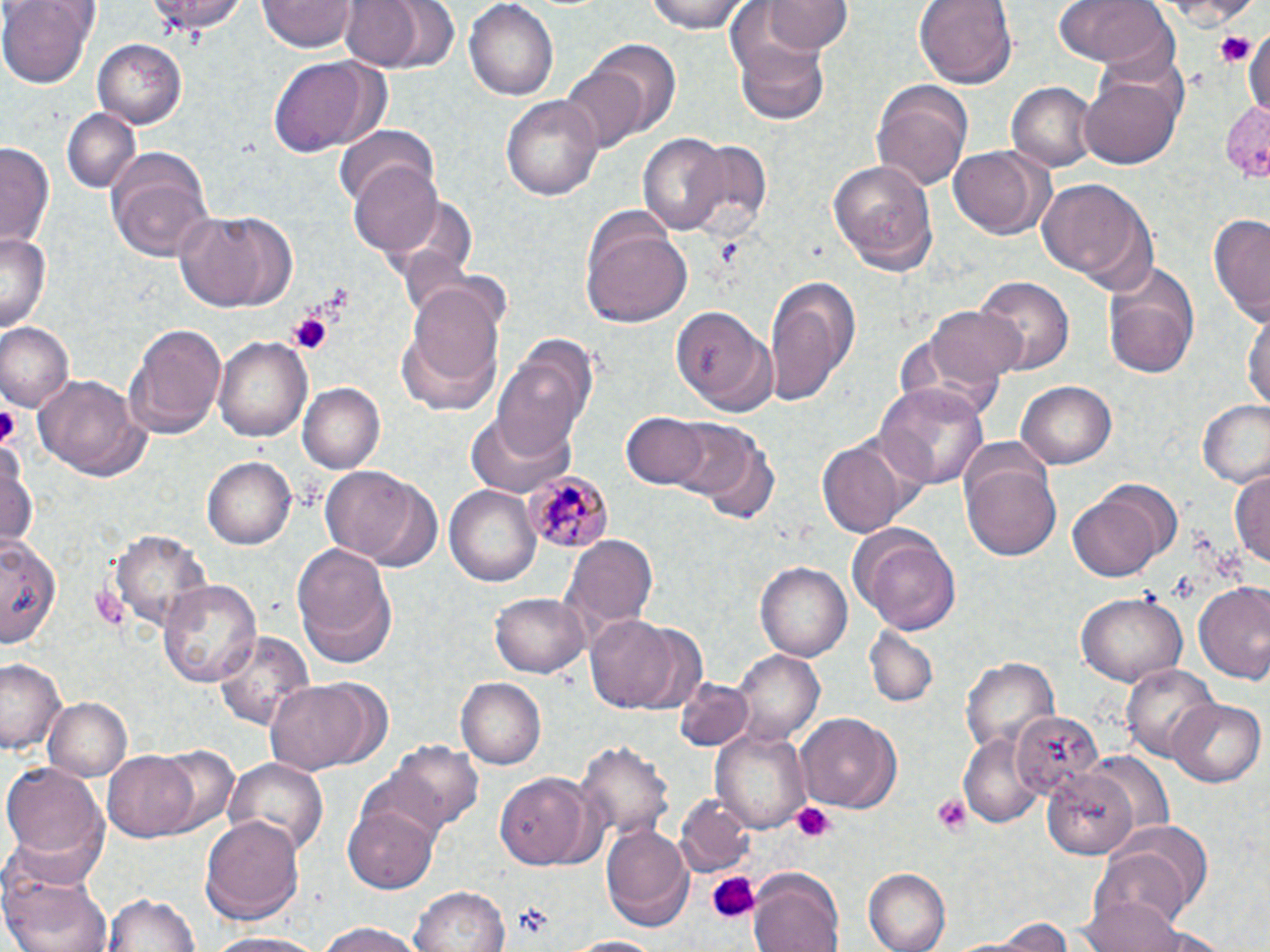

slide-level diagnosis = Plasmodium malariae
uninfected red blood cell locations = approximate bounding boxes as (x1,y1)-(x2,y2) corner pairs in pixels: (0,0)-(95,88), (148,0)-(247,36), (262,0)-(356,52), (339,0)-(454,73), (643,0)-(756,33), (765,0)-(850,54), (917,0)-(1015,89), (1056,0)-(1178,71), (1138,1)-(1267,28), (463,2)-(559,102), (1244,20)-(1270,125), (737,36)-(830,124), (92,38)-(187,129), (578,39)-(679,144), (265,53)-(381,159), (562,65)-(646,151), (1080,75)-(1181,168), (871,80)-(973,191), (1008,80)-(1098,172), (500,93)-(604,200), (1217,101)-(1270,185), (61,108)-(142,195), (334,127)-(440,213), (639,132)-(729,236), (680,137)-(772,243), (1,140)-(55,251), (105,146)-(216,263), (948,146)-(1054,240), (348,160)-(446,256), (828,160)-(940,276), (1036,178)-(1157,293), (174,210)-(297,310), (582,212)-(692,329), (1208,214)-(1270,328), (0,231)-(49,335), (1104,260)-(1199,379), (765,275)-(859,406), (974,277)-(1073,380), (404,280)-(502,399), (923,301)-(1024,396), (669,304)-(774,416), (1244,307)-(1269,416), (124,320)-(226,438), (0,322)-(74,412), (214,334)-(312,444), (494,340)-(597,457), (31,372)-(151,484), (1017,381)-(1116,469), (298,382)-(384,474), (875,382)-(991,491), (1198,400)-(1270,486), (465,413)-(574,499), (623,413)-(711,489), (660,419)-(758,503), (819,435)-(911,539), (1,439)-(39,554), (699,439)-(780,525), (201,454)-(295,549), (964,461)-(1061,561), (322,466)-(425,565), (1231,466)-(1270,575), (446,484)-(542,586), (1066,491)-(1166,582), (850,527)-(962,634), (110,529)-(213,635), (0,535)-(65,652), (564,535)-(659,631), (294,544)-(393,650), (756,560)-(852,664), (158,579)-(262,690), (1195,583)-(1270,686), (1077,592)-(1186,685), (490,594)-(588,680), (587,615)-(685,712), (212,628)-(316,735), (865,628)-(938,708), (736,651)-(824,743), (962,655)-(1057,756), (2,659)-(65,759), (1120,662)-(1218,764), (261,678)-(383,777), (456,678)-(545,768), (674,678)-(756,751), (1167,697)-(1264,787), (43,698)-(133,782), (1010,711)-(1104,802), (796,712)-(901,812), (711,728)-(810,831), (959,733)-(1042,825), (578,739)-(673,842), (387,742)-(484,832), (152,744)-(237,834), (104,751)-(201,841), (227,760)-(327,858), (5,764)-(106,866), (1043,770)-(1138,862), (496,773)-(604,873), (676,796)-(754,877), (344,801)-(438,893), (202,814)-(305,921), (599,820)-(692,927), (1093,835)-(1204,935), (1,864)-(112,952), (748,868)-(846,952), (866,868)-(951,952), (410,886)-(509,952), (102,890)-(199,952), (1085,896)-(1190,952), (976,914)-(1081,951), (313,922)-(426,952), (207,931)-(326,951), (561,935)-(670,952)
field of view = single
magnification = 1000x
image size = 1270×952 pixels
Plasmodium malariae-infected red blood cell locations = approximate bounding boxes as (x1,y1)-(x2,y2) corner pairs in pixels: (524,471)-(613,553)
preparation = thin blood film
platelet locations = approximate bounding boxes as (x1,y1)-(x2,y2) corner pairs in pixels: (1212,29)-(1258,70), (286,311)-(332,355), (0,405)-(17,443), (1169,570)-(1199,604), (930,794)-(974,836), (791,802)-(836,844), (707,873)-(761,922), (513,904)-(552,938)
modality = light microscopy
stain = May-Grünwald-Giemsa